Classify this cell by malaria status.
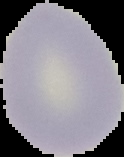

It is uninfected.

Segmented cell region on a black background. Image is 124×157 pixels. From a thin blood film.